Outline each blood parasite and name the species.
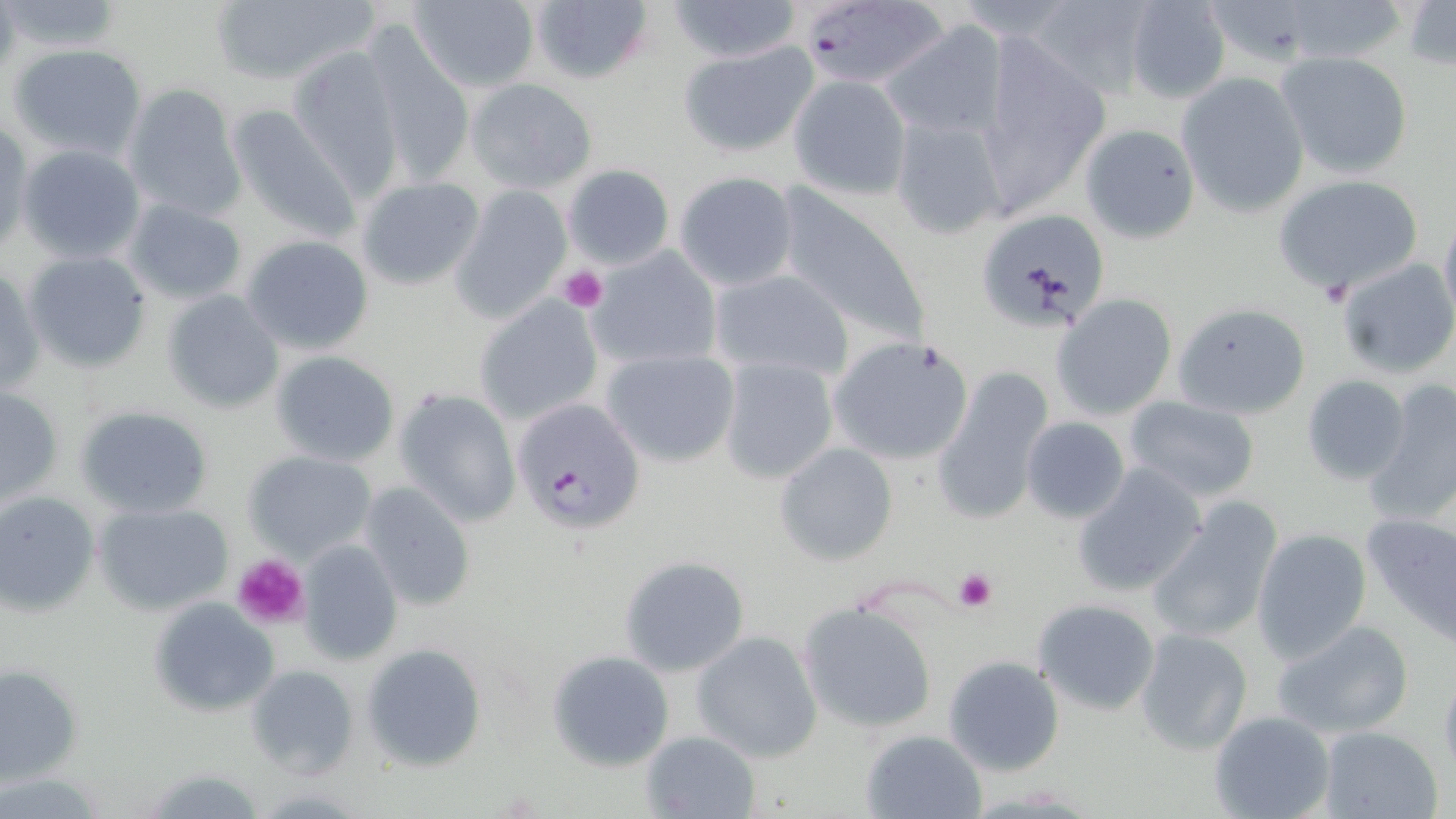

Approximate bounding boxes as named x1/y1/x2/y2 corners in pixels.
Plasmodium falciparum-infected red blood cells: (x1=797, y1=0, x2=954, y2=94), (x1=516, y1=402, x2=642, y2=535).
No Plasmodium ovale, Plasmodium malariae, Plasmodium vivax, Babesia divergens, or Trypanosoma brucei observed.

slide_level_diagnosis: Plasmodium falciparum
platelet_locations: 'approximate bounding boxes as named x1/y1/x2/y2 corners in pixels: (x1=558, y1=266, x2=606, y2=310), (x1=1319, y1=280, x2=1352, y2=309), (x1=231, y1=552, x2=310, y2=629), (x1=953, y1=567, x2=998, y2=612)'
stain: May-Grünwald-Giemsa
magnification: 1000x
preparation: thin blood smear
uninfected_red_blood_cell_locations: 'approximate bounding boxes as named x1/y1/x2/y2 corners in pixels: (x1=206, y1=0, x2=379, y2=88), (x1=407, y1=0, x2=541, y2=93), (x1=530, y1=0, x2=656, y2=87), (x1=665, y1=0, x2=805, y2=63), (x1=1027, y1=0, x2=1155, y2=99), (x1=1123, y1=0, x2=1231, y2=103), (x1=1402, y1=0, x2=1455, y2=72), (x1=880, y1=21, x2=1009, y2=140), (x1=361, y1=24, x2=474, y2=186), (x1=973, y1=31, x2=1109, y2=213), (x1=679, y1=41, x2=820, y2=160), (x1=7, y1=42, x2=148, y2=161), (x1=286, y1=44, x2=404, y2=198), (x1=1273, y1=50, x2=1415, y2=180), (x1=1175, y1=72, x2=1311, y2=217), (x1=788, y1=74, x2=911, y2=199), (x1=467, y1=78, x2=598, y2=194), (x1=122, y1=84, x2=246, y2=221), (x1=224, y1=104, x2=362, y2=246), (x1=889, y1=112, x2=1012, y2=242), (x1=1, y1=121, x2=32, y2=254), (x1=1080, y1=123, x2=1201, y2=242), (x1=17, y1=144, x2=146, y2=265), (x1=563, y1=163, x2=675, y2=271), (x1=674, y1=170, x2=800, y2=289), (x1=1274, y1=173, x2=1426, y2=295), (x1=354, y1=176, x2=485, y2=289), (x1=449, y1=185, x2=571, y2=322), (x1=773, y1=186, x2=929, y2=346), (x1=124, y1=198, x2=249, y2=304), (x1=975, y1=208, x2=1110, y2=332), (x1=1439, y1=210, x2=1456, y2=331), (x1=243, y1=235, x2=375, y2=356), (x1=587, y1=244, x2=722, y2=369), (x1=24, y1=250, x2=153, y2=373), (x1=1335, y1=258, x2=1456, y2=377), (x1=0, y1=264, x2=43, y2=400), (x1=711, y1=268, x2=853, y2=382), (x1=162, y1=290, x2=285, y2=415), (x1=1051, y1=294, x2=1179, y2=420), (x1=474, y1=295, x2=604, y2=428), (x1=1173, y1=302, x2=1311, y2=419), (x1=827, y1=334, x2=976, y2=466), (x1=601, y1=348, x2=740, y2=467), (x1=269, y1=351, x2=400, y2=466), (x1=718, y1=357, x2=839, y2=484), (x1=931, y1=366, x2=1057, y2=526), (x1=1301, y1=375, x2=1411, y2=485), (x1=1363, y1=381, x2=1456, y2=526), (x1=0, y1=385, x2=62, y2=508), (x1=394, y1=387, x2=520, y2=528), (x1=1121, y1=397, x2=1262, y2=503), (x1=74, y1=404, x2=214, y2=519), (x1=1021, y1=416, x2=1131, y2=523), (x1=774, y1=442, x2=899, y2=566), (x1=246, y1=450, x2=376, y2=564), (x1=1073, y1=463, x2=1208, y2=597), (x1=359, y1=480, x2=476, y2=611), (x1=0, y1=492, x2=100, y2=614), (x1=1146, y1=499, x2=1284, y2=646), (x1=93, y1=502, x2=235, y2=615), (x1=1361, y1=514, x2=1456, y2=640), (x1=1250, y1=528, x2=1372, y2=662), (x1=298, y1=540, x2=403, y2=666), (x1=617, y1=556, x2=750, y2=678), (x1=1032, y1=597, x2=1162, y2=715), (x1=148, y1=598, x2=278, y2=717), (x1=794, y1=599, x2=940, y2=734), (x1=1038, y1=612, x2=1252, y2=739), (x1=1270, y1=619, x2=1415, y2=740), (x1=1134, y1=628, x2=1254, y2=756), (x1=690, y1=631, x2=823, y2=762), (x1=362, y1=644, x2=487, y2=772), (x1=547, y1=651, x2=674, y2=771), (x1=942, y1=654, x2=1063, y2=777), (x1=1, y1=664, x2=82, y2=784), (x1=1438, y1=664, x2=1456, y2=782), (x1=245, y1=665, x2=358, y2=779), (x1=1208, y1=710, x2=1335, y2=819), (x1=1316, y1=726, x2=1444, y2=819), (x1=861, y1=729, x2=986, y2=818), (x1=641, y1=731, x2=762, y2=819), (x1=136, y1=765, x2=271, y2=818)'
field_of_view: one of a larger specimen
modality: optical microscopy
image_size: 1456×819 pixels